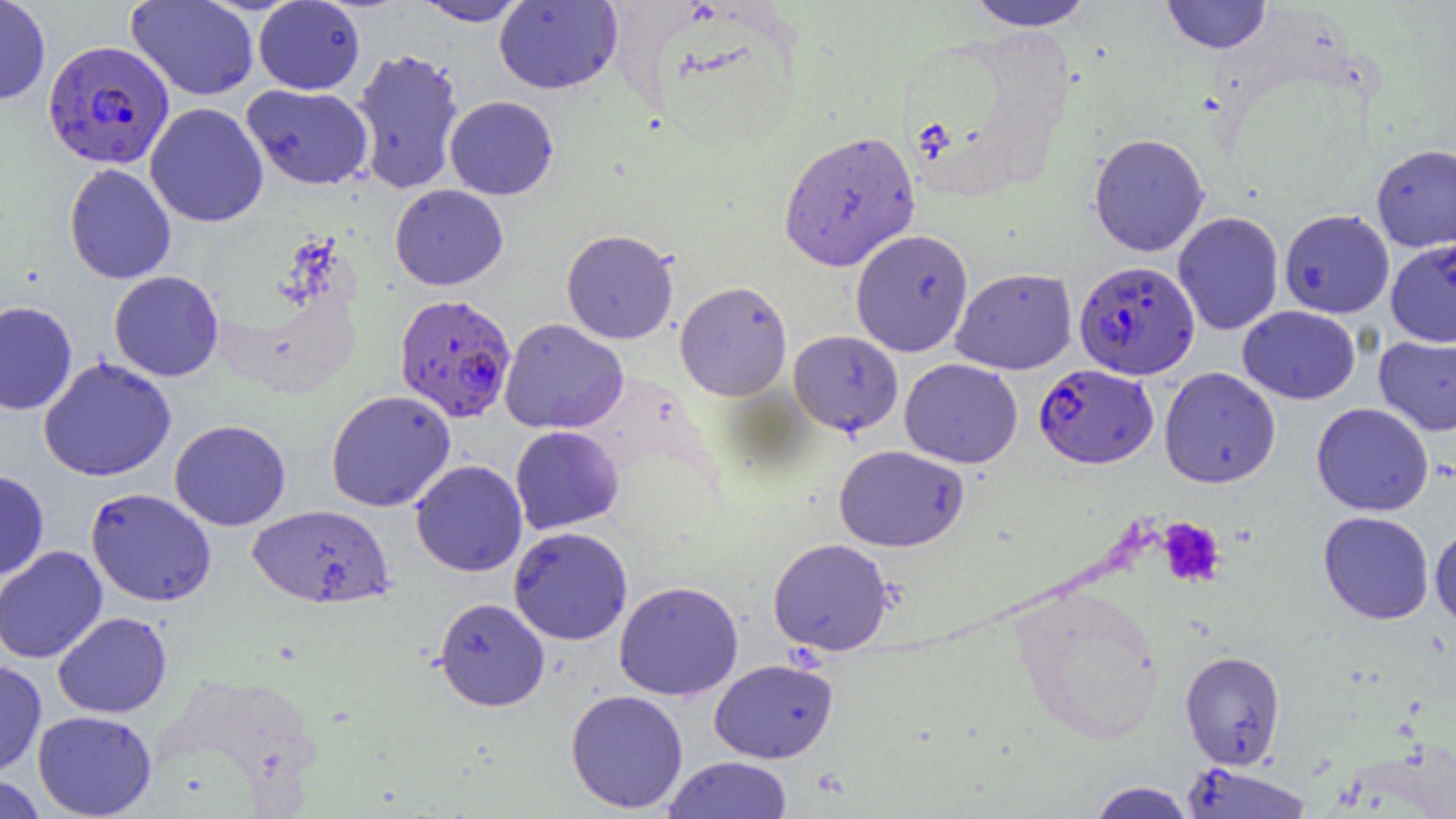

{
  "slide_level_diagnosis": "Plasmodium falciparum",
  "magnification": "1000x",
  "image_size": "1456×819 pixels",
  "uninfected_red_blood_cell_locations": "approximate bounding boxes as [x1, y1, x2, y2] in pixels: [0, 0, 51, 104], [126, 0, 259, 101], [964, 0, 1095, 31], [1162, 0, 1271, 53], [254, 1, 365, 95], [414, 1, 531, 26], [494, 1, 623, 94], [351, 47, 464, 195], [241, 83, 374, 190], [445, 95, 558, 199], [144, 102, 268, 227], [779, 129, 920, 272], [1089, 133, 1209, 256], [1371, 143, 1456, 252], [64, 163, 177, 284], [390, 184, 508, 290], [1279, 209, 1394, 318], [1173, 211, 1284, 336], [851, 228, 974, 357], [561, 229, 678, 344], [1386, 237, 1456, 347], [951, 268, 1077, 375], [109, 271, 224, 381], [675, 280, 792, 401], [0, 301, 77, 414], [1238, 305, 1360, 404], [499, 318, 628, 434], [789, 331, 903, 436], [1374, 332, 1456, 436], [38, 357, 176, 482], [900, 358, 1022, 468], [1160, 367, 1281, 488], [326, 389, 456, 512], [1312, 402, 1434, 516], [169, 420, 291, 531], [510, 425, 624, 534], [834, 444, 968, 551], [411, 460, 527, 576], [0, 470, 49, 580], [85, 487, 216, 607], [248, 504, 395, 609], [1318, 511, 1434, 624], [1430, 523, 1456, 630], [509, 526, 633, 645], [768, 538, 893, 655], [0, 545, 107, 664], [614, 581, 743, 701], [1012, 582, 1163, 743], [435, 597, 550, 711], [53, 612, 172, 718], [1180, 650, 1285, 769], [709, 658, 838, 763], [0, 659, 47, 779], [566, 689, 688, 813], [34, 710, 157, 818], [663, 755, 793, 818], [1180, 762, 1315, 818], [0, 774, 47, 819], [1086, 781, 1196, 818]",
  "modality": "light microscopy",
  "preparation": "thin blood film",
  "plasmodium_falciparum_infected_red_blood_cell_locations": "approximate bounding boxes as [x1, y1, x2, y2] in pixels: [43, 40, 174, 169], [1074, 260, 1199, 379], [394, 293, 516, 423], [1034, 363, 1159, 468]",
  "field_of_view": "one of a larger specimen",
  "platelet_locations": "approximate bounding boxes as [x1, y1, x2, y2] in pixels: [1158, 519, 1225, 587]"
}